Assess the morphology of the red blood cells.
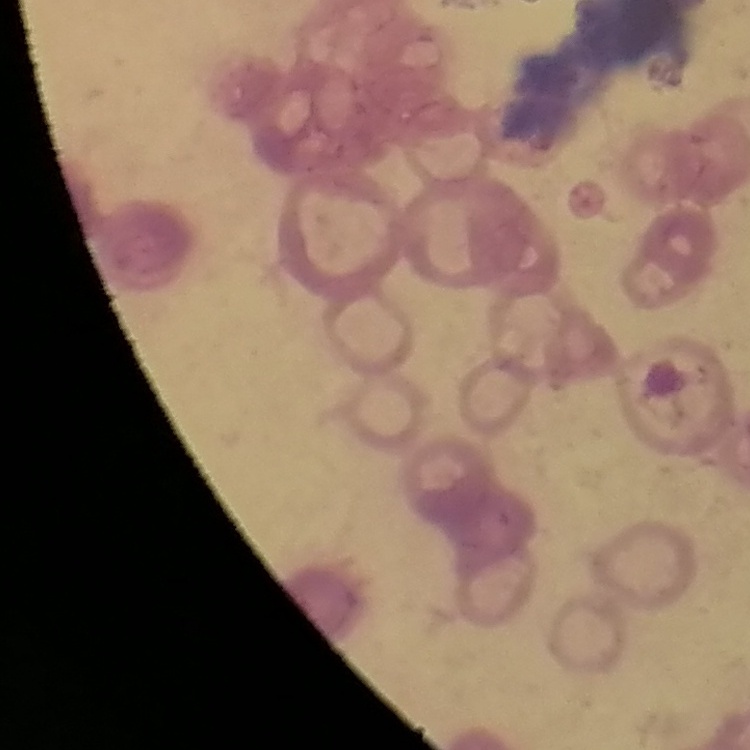

They show rouleaux formation.

stain = Field's or Giemsa
image type = square crop of a larger photomicrograph
preparation = thin peripheral smear